Assess this cell for malaria.
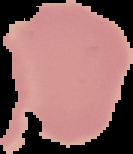

It is uninfected.

From a thin blood smear. Image is 133×154 pixels. Cell region segmented out of the field of view; the surrounding area is masked to black.